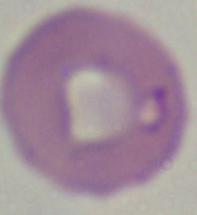
Summary:
  - Magnification: 1000x
  - Identification: Babesia
  - Modality: photomicrograph